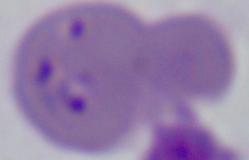 1000x magnification. Micrograph. A Babesia parasite is shown.